Assess this cell for malaria.
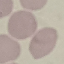
It is uninfected.

image type = cell patch, automatically extracted from a larger field of view and resized to 64 × 64 pixels
stain = Giemsa
capture = smartphone camera at the microscope eyepiece
preparation = thin blood smear